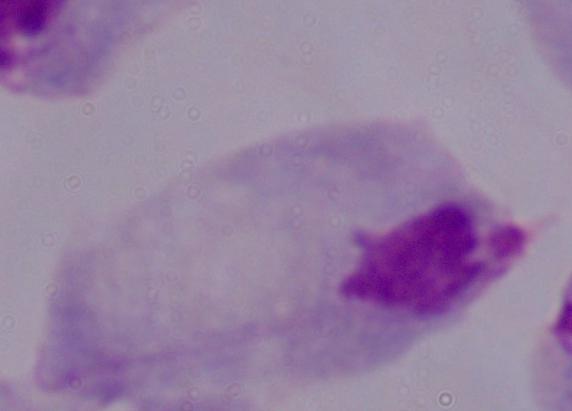

Summary:
  - Identification: trichomonad
  - Modality: photomicrograph
  - Magnification: 1000x